Classify this cell by malaria status.
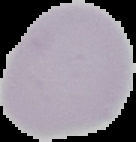
Uninfected.

Cell region segmented out of the field of view; the surrounding area is masked to black. From a thin blood film. Image is 136×142 pixels.